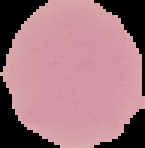

Image is 145×148 pixels. From a thin blood smear. Cell region segmented out of the field of view; the surrounding area is masked to black. Result: no Plasmodium parasites detected.